Locate every blood parasite and identify its species.
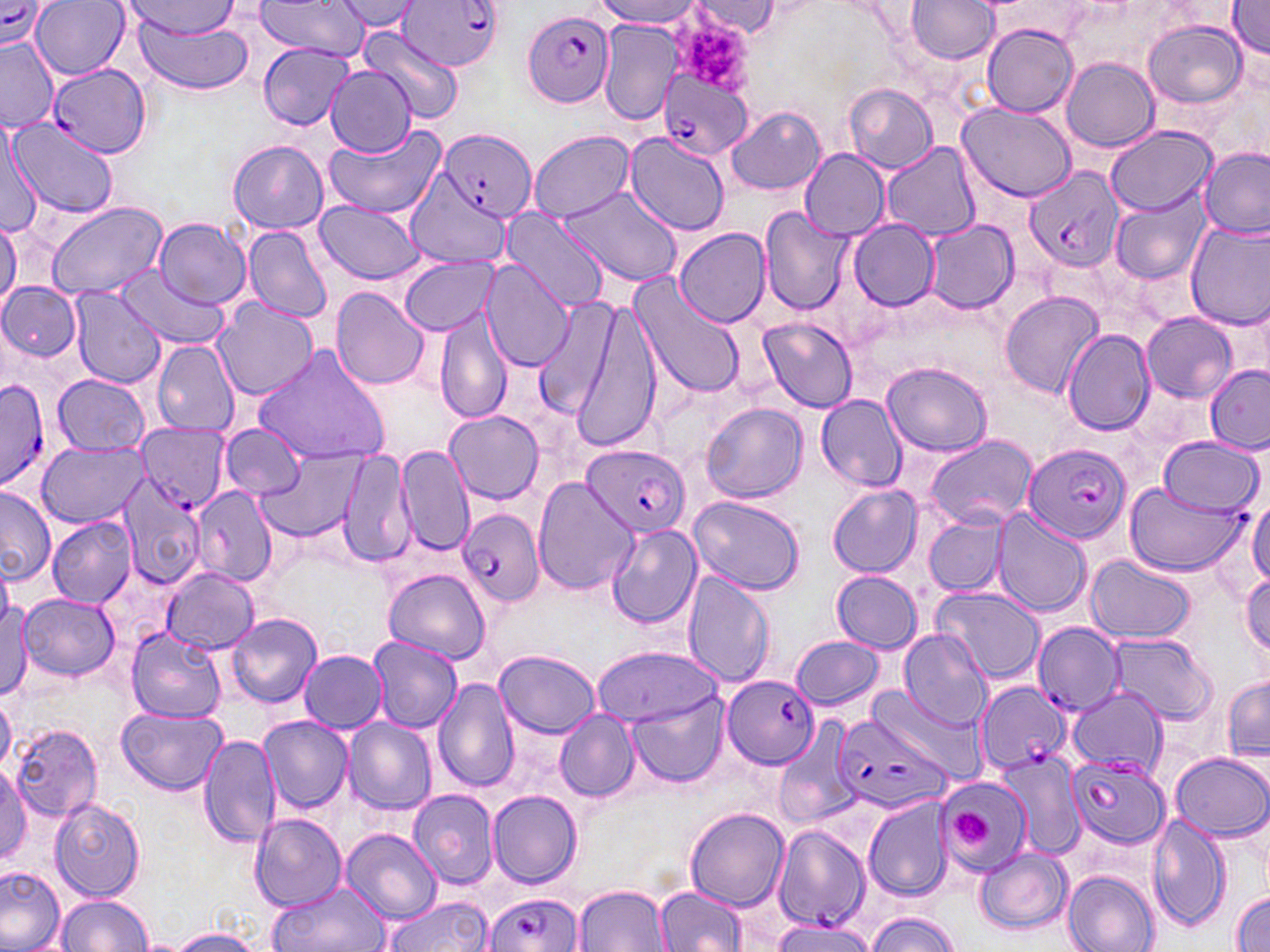
Approximate bounding boxes as (x1,y1)-(x2,y2) corner pairs in pixels.
Plasmodium falciparum-infected red blood cells: (398,0)-(505,71), (0,1)-(53,49), (522,9)-(614,107), (48,62)-(151,156), (660,71)-(752,161), (438,130)-(536,222), (1023,165)-(1124,275), (0,378)-(53,492), (138,427)-(229,507), (1023,443)-(1133,544), (584,445)-(691,536), (457,506)-(546,608), (1032,622)-(1124,715), (723,674)-(819,768), (974,682)-(1069,775), (832,711)-(957,816), (1068,752)-(1171,848), (771,822)-(875,929), (482,893)-(581,952).
No Plasmodium ovale, Plasmodium malariae, Plasmodium vivax, Babesia divergens, or Trypanosoma brucei observed.

Platelet locations: (672,10)-(754,95), (952,809)-(991,846). Uninfected red blood cell locations: (32,0)-(131,79), (597,0)-(702,27), (904,0)-(1001,65), (121,1)-(245,43), (253,1)-(368,60), (336,1)-(421,31), (691,2)-(783,37), (1226,2)-(1270,60), (131,15)-(257,94), (598,20)-(682,125), (1143,20)-(1249,109), (981,23)-(1079,117), (360,26)-(463,124), (1,37)-(61,132), (257,42)-(355,129), (1061,58)-(1159,151), (324,64)-(416,158), (845,83)-(938,172), (957,102)-(1076,201), (726,107)-(825,196), (6,117)-(119,221), (0,121)-(42,234), (324,123)-(446,218), (1108,126)-(1217,214), (530,130)-(633,222), (623,131)-(731,236), (228,141)-(329,233), (883,143)-(979,239), (1200,147)-(1270,239), (801,150)-(890,240), (405,173)-(510,268), (560,184)-(681,286), (1110,193)-(1211,285), (313,199)-(425,284), (45,201)-(165,297), (760,208)-(852,316), (499,210)-(610,316), (155,217)-(251,310), (923,218)-(1018,314), (0,219)-(20,309), (848,220)-(940,310), (1186,222)-(1270,329), (243,225)-(334,324), (674,226)-(771,328), (403,256)-(496,334), (480,261)-(576,372), (114,266)-(228,349), (630,272)-(746,399), (1,282)-(82,361), (69,287)-(165,389), (331,287)-(431,391), (1000,291)-(1103,399), (531,298)-(618,416), (211,300)-(319,404), (569,300)-(661,455), (437,302)-(514,425), (1141,313)-(1237,403), (758,318)-(858,412), (1062,327)-(1156,435), (151,341)-(240,435), (253,344)-(392,467), (882,363)-(992,456), (1204,364)-(1270,451), (53,374)-(150,455), (816,395)-(908,491), (702,403)-(808,502), (445,410)-(543,504), (220,423)-(306,502), (924,435)-(1037,530), (1157,436)-(1265,516), (37,443)-(151,528), (253,445)-(369,542), (395,446)-(474,554), (338,449)-(415,569), (114,474)-(205,592), (533,478)-(639,595), (1123,480)-(1249,575), (193,485)-(276,585), (0,486)-(55,585), (828,486)-(923,577), (688,495)-(805,595), (1247,497)-(1270,590), (990,511)-(1088,617), (923,513)-(1008,597), (46,515)-(138,606), (607,524)-(702,629), (622,537)-(759,653), (1086,555)-(1197,644), (161,566)-(259,654), (384,567)-(492,663), (832,570)-(923,652), (681,571)-(774,686), (1240,574)-(1270,658), (930,587)-(1047,684), (19,593)-(120,681), (0,594)-(32,701), (225,613)-(322,708), (126,626)-(228,724), (899,628)-(994,731), (1108,632)-(1215,724), (790,635)-(885,711), (367,636)-(461,733), (593,645)-(721,726), (299,649)-(387,732), (494,649)-(600,739), (433,675)-(519,794), (1222,678)-(1270,764), (1065,686)-(1167,773), (870,687)-(986,786), (0,696)-(14,773), (627,696)-(729,787), (119,705)-(226,795), (554,711)-(640,801), (259,716)-(353,813), (343,718)-(438,816), (771,719)-(859,831), (11,722)-(103,823), (198,734)-(280,847), (995,749)-(1087,859), (1170,751)-(1269,842), (0,766)-(32,863), (935,779)-(1028,881), (408,790)-(498,890), (488,790)-(582,888), (864,795)-(958,901), (50,798)-(146,901), (685,808)-(790,912), (1147,812)-(1231,933), (250,814)-(347,912), (341,828)-(442,924), (975,847)-(1072,934), (0,864)-(65,952), (1063,869)-(1160,952), (267,880)-(392,952), (575,884)-(672,952), (655,885)-(749,952), (1230,892)-(1270,950), (55,895)-(152,951), (382,895)-(493,952), (864,912)-(962,952), (768,917)-(879,951), (166,929)-(264,952). Slide-level diagnosis: Plasmodium falciparum. May-Grünwald-Giemsa-stained preparation. Thin blood smear. Image is 1270×952 pixels. 1000x magnification. Optical microscopy. Single field of view.